Assess the morphology of the red blood cells.
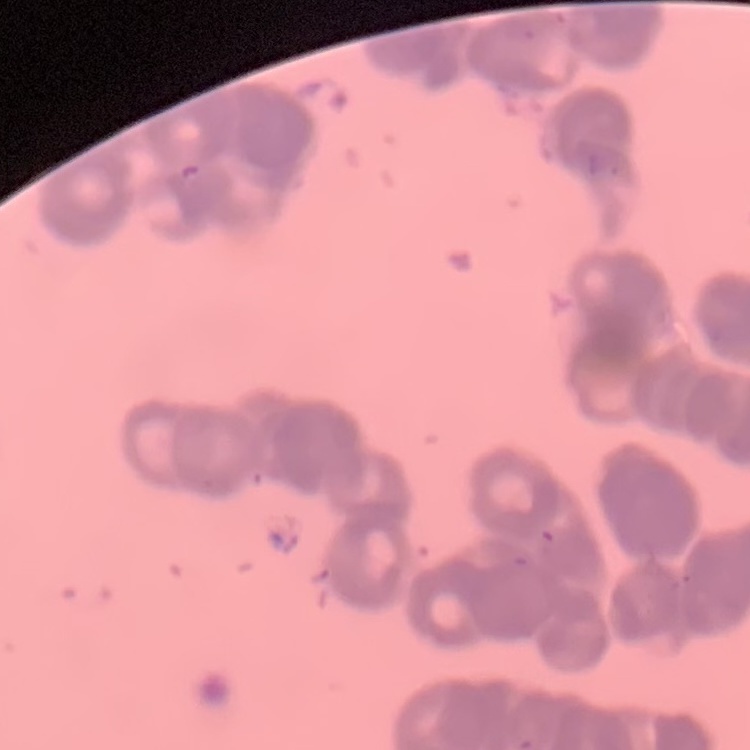

Rouleaux formation.

Summary:
  - Preparation: thin blood film
  - Image type: square crop of a larger photomicrograph
  - Stain: Field's or Giemsa